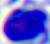
Photomicrograph. A white blood cell is seen. Captured at 400x magnification.